Give the position of every Plasmodium parasite visible.
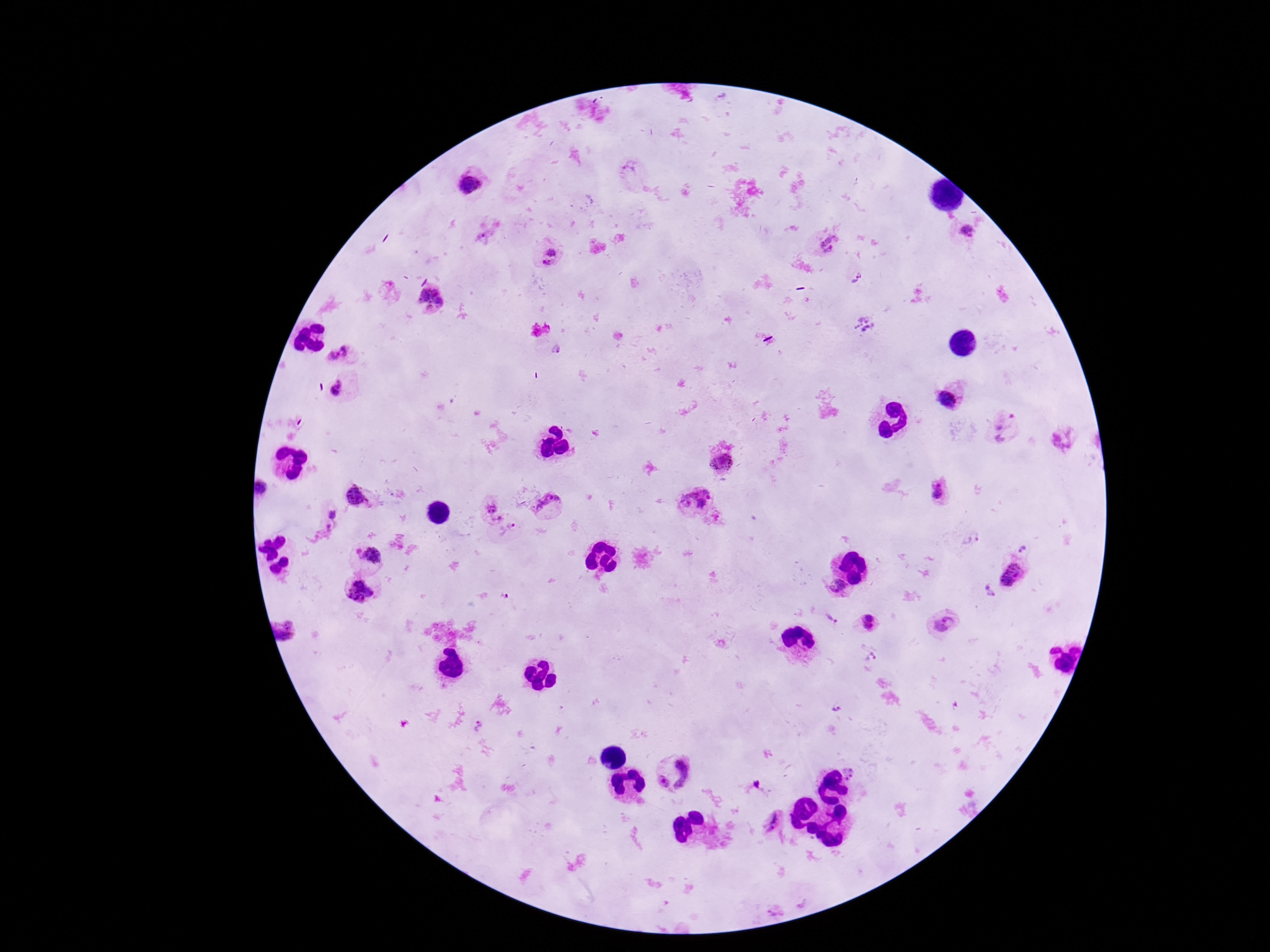
Approximate centers as {x, y} in pixels.
Plasmodium parasites: {631, 167}, {466, 185}, {967, 229}, {484, 236}, {830, 245}, {550, 258}, {857, 278}, {428, 301}, {867, 324}, {555, 349}, {340, 354}, {338, 387}, {947, 395}, {1003, 426}, {1064, 438}, {722, 460}, {264, 488}, {940, 490}, {358, 496}, {700, 504}, {492, 508}, {552, 510}, {330, 512}, {510, 531}, {1023, 548}, {373, 555}, {1014, 575}, {837, 587}, {988, 592}, {360, 593}, {831, 620}, {868, 624}, {942, 624}, {283, 630}, {870, 658}, {840, 708}, {478, 728}, {850, 773}, {758, 784}, {775, 822}.

preparation = thick peripheral-blood smear
image size = 1270×952 pixels
magnification = 100x
capture = smartphone camera through the microscope eyepiece
patient malaria status = infected
field of view = one from this slide
stain = Giemsa